Locate and identify every blood parasite.
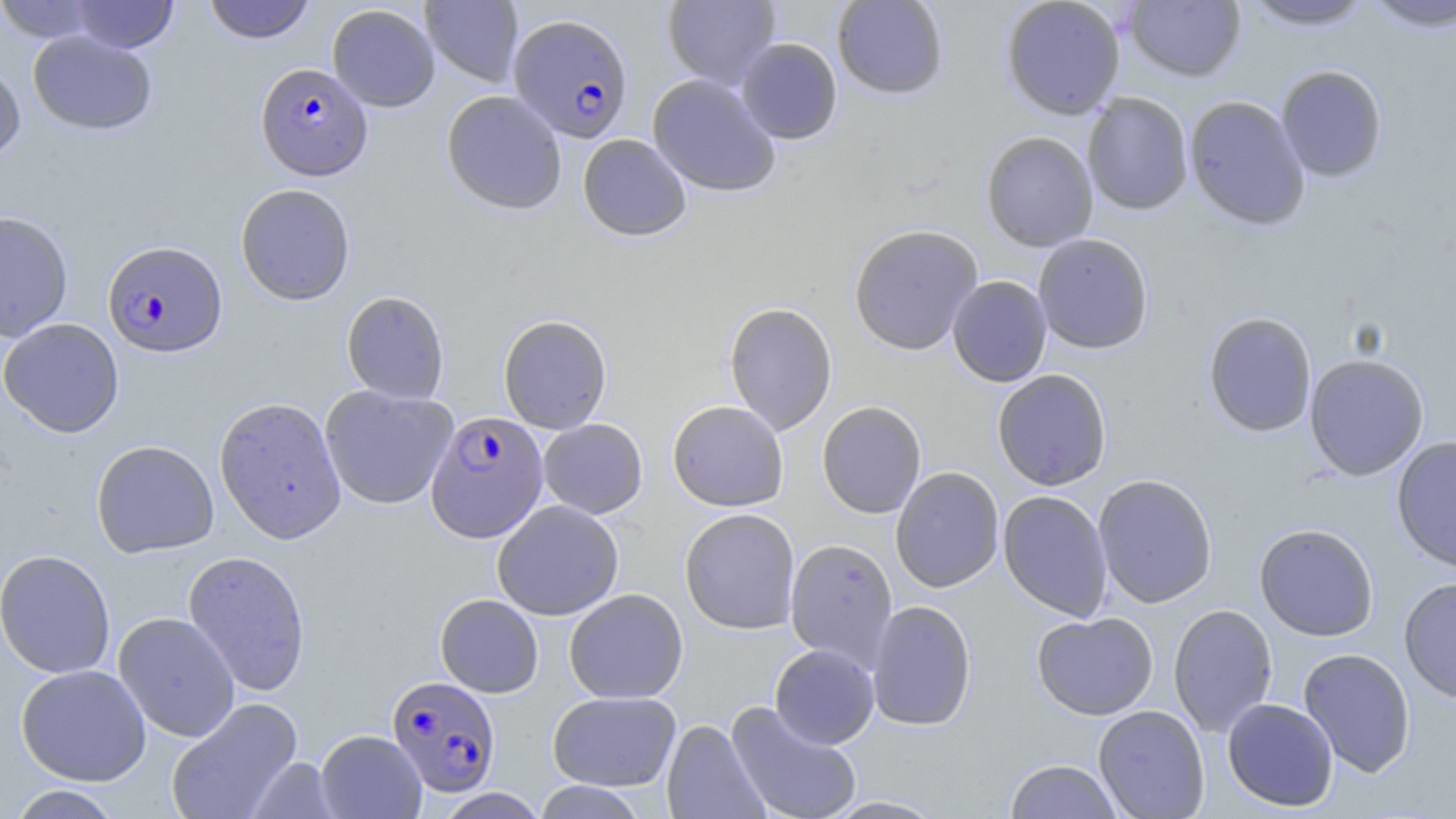

Approximate bounding boxes as [x1, y1, x2, y2] in pixels.
Plasmodium falciparum-infected red blood cells: [508, 13, 633, 142], [255, 62, 372, 181], [102, 241, 228, 359], [425, 410, 548, 543], [387, 675, 501, 797].
No Plasmodium ovale, Plasmodium malariae, Plasmodium vivax, Babesia divergens, or Trypanosoma brucei observed.

{
  "slide_level_diagnosis": "Plasmodium falciparum",
  "uninfected_red_blood_cell_locations": "approximate bounding boxes as [x1, y1, x2, y2] in pixels: [0, 0, 106, 43], [67, 0, 179, 53], [202, 0, 316, 45], [420, 0, 524, 87], [662, 0, 781, 89], [832, 0, 948, 99], [1001, 0, 1126, 119], [1125, 0, 1245, 83], [1361, 0, 1456, 32], [1239, 1, 1376, 31], [327, 4, 440, 112], [27, 30, 157, 135], [736, 38, 843, 144], [0, 60, 26, 164], [1276, 64, 1388, 182], [647, 73, 782, 197], [441, 90, 567, 215], [1082, 92, 1193, 215], [1185, 96, 1310, 231], [981, 131, 1098, 251], [577, 134, 692, 241], [235, 183, 356, 306], [0, 210, 74, 343], [848, 223, 983, 355], [1033, 233, 1154, 354], [947, 276, 1052, 387], [341, 290, 450, 405], [723, 302, 838, 436], [1203, 311, 1317, 438], [498, 314, 612, 434], [0, 318, 124, 438], [1304, 353, 1429, 481], [992, 369, 1112, 491], [319, 385, 458, 510], [214, 396, 347, 544], [667, 400, 788, 512], [817, 401, 927, 519], [538, 418, 648, 519], [1391, 436, 1456, 573], [91, 440, 219, 559], [890, 466, 1004, 592], [1093, 473, 1218, 608], [997, 490, 1113, 622], [492, 500, 624, 621], [679, 508, 800, 635], [1254, 523, 1379, 641], [785, 538, 898, 669], [0, 549, 116, 679], [183, 550, 312, 697], [1398, 576, 1456, 703], [564, 588, 688, 704], [435, 594, 544, 697], [866, 600, 977, 731], [1168, 604, 1278, 738], [113, 612, 240, 742], [1032, 612, 1158, 720], [769, 644, 880, 749], [1298, 648, 1416, 777], [15, 664, 152, 786], [547, 691, 681, 791], [165, 697, 303, 819], [1222, 697, 1338, 812], [725, 701, 863, 819], [1093, 705, 1210, 819], [661, 719, 770, 819], [315, 729, 427, 819], [247, 757, 342, 818], [1005, 759, 1122, 818], [531, 781, 649, 818], [5, 785, 127, 818], [818, 795, 949, 818]",
  "preparation": "thin blood film",
  "field_of_view": "one of a larger specimen",
  "magnification": "1000x",
  "modality": "light microscopy",
  "image_size": "1456×819 pixels",
  "stain": "May-Grünwald-Giemsa"
}